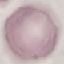 Malaria status: uninfected. Photographed with a smartphone camera at the microscope eyepiece. Giemsa-stained preparation. Thin blood smear. Cell patch, automatically extracted from a larger field of view and resized to 64 × 64 pixels.